Assess this cell for malaria.
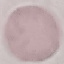
Uninfected.

stain = Giemsa
image type = cell patch, automatically extracted from a larger field of view and resized to 64 × 64 pixels
preparation = thin blood smear
capture = smartphone camera at the microscope eyepiece